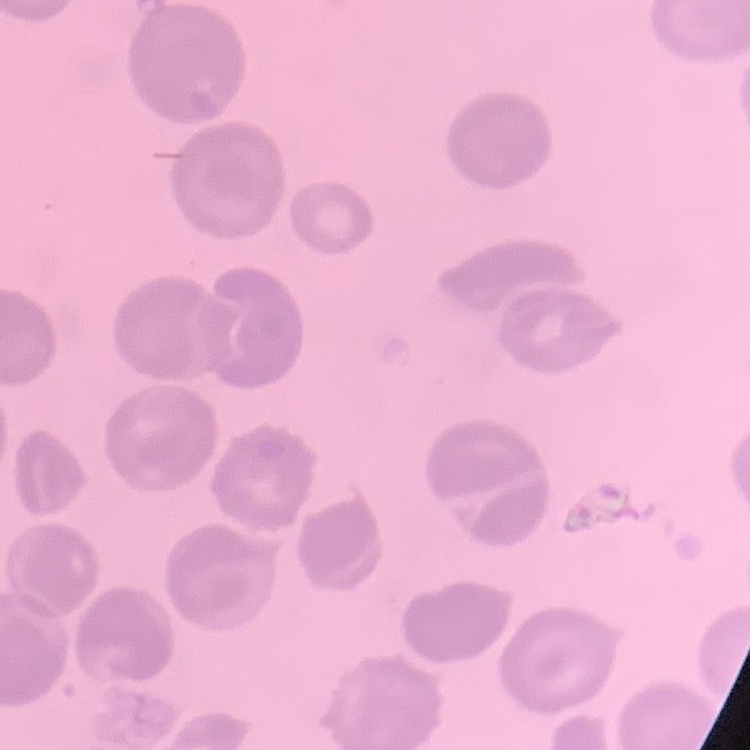

{
  "erythrocyte_morphology": "no rouleaux formation",
  "preparation": "thin peripheral smear",
  "image_type": "one tile cut from a larger photomicrograph",
  "stain": "Field's or Giemsa"
}